Report the malaria status of this cell.
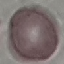

Uninfected.

Automatically extracted cell patch, resized to 64 × 64 pixels. Thin blood film. Acquired by smartphone through the microscope eyepiece. Giemsa-stained preparation.